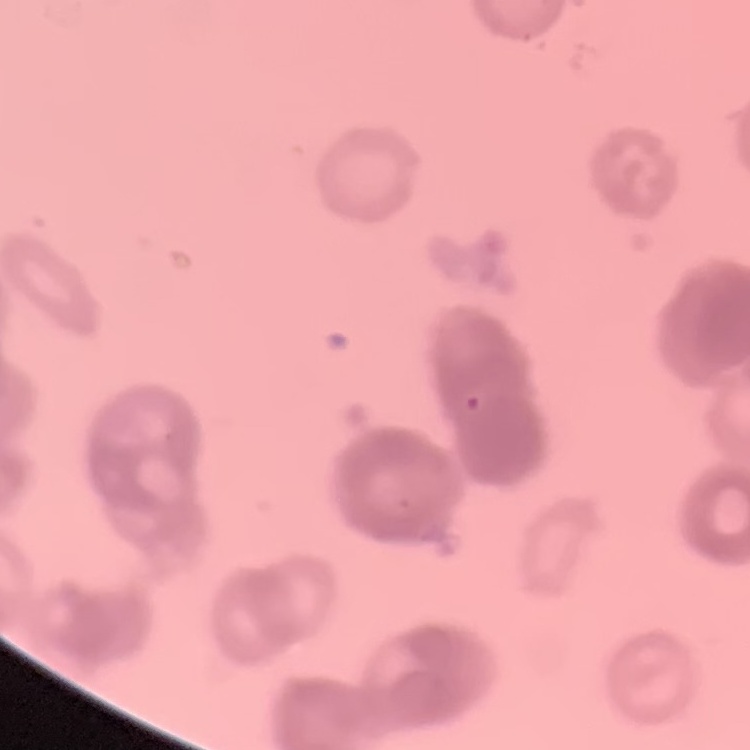

erythrocyte morphology = rouleaux formation
image type = one tile cut from a larger photomicrograph
stain = Field's or Giemsa
preparation = thin peripheral smear